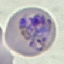
result = malaria parasites detected
preparation = thin blood film
capture = smartphone camera at the microscope eyepiece
image type = cell patch, automatically extracted from a larger field of view and resized to 64 × 64 pixels
stain = Giemsa